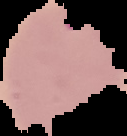

Summary:
  - Malaria status: parasitized
  - Image size: 127×136 pixels
  - Preparation: thin blood smear
  - Image type: segmented cell region on a black background